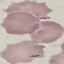

Malaria status: uninfected. Giemsa stain. Thin smear of blood. Photographed with a smartphone camera at the microscope eyepiece. Automatically extracted cell patch, resized to 64 × 64 pixels.